Assess the morphology of the erythrocytes.
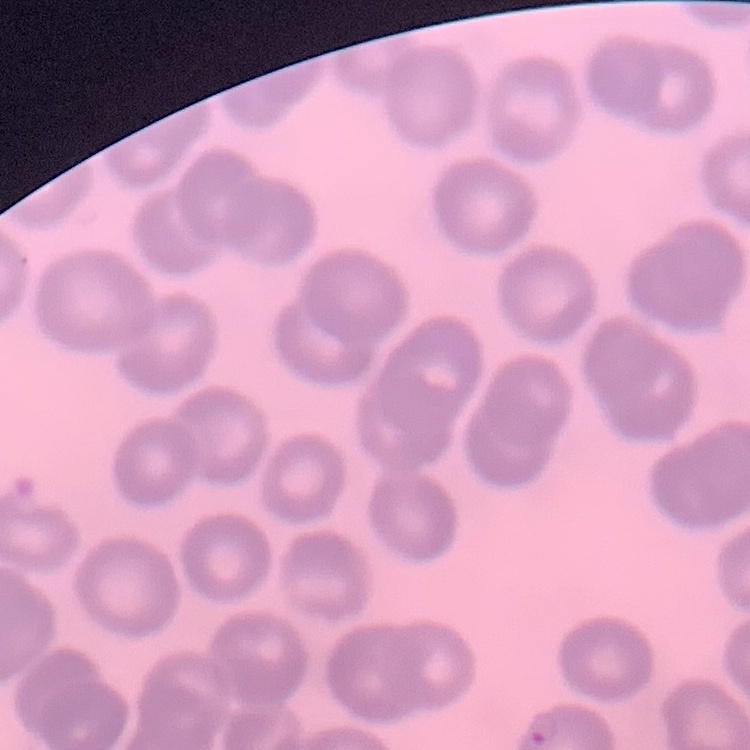
No rouleaux formation.

One tile cut from a larger photomicrograph. Field's or Giemsa stain. Thin blood smear.